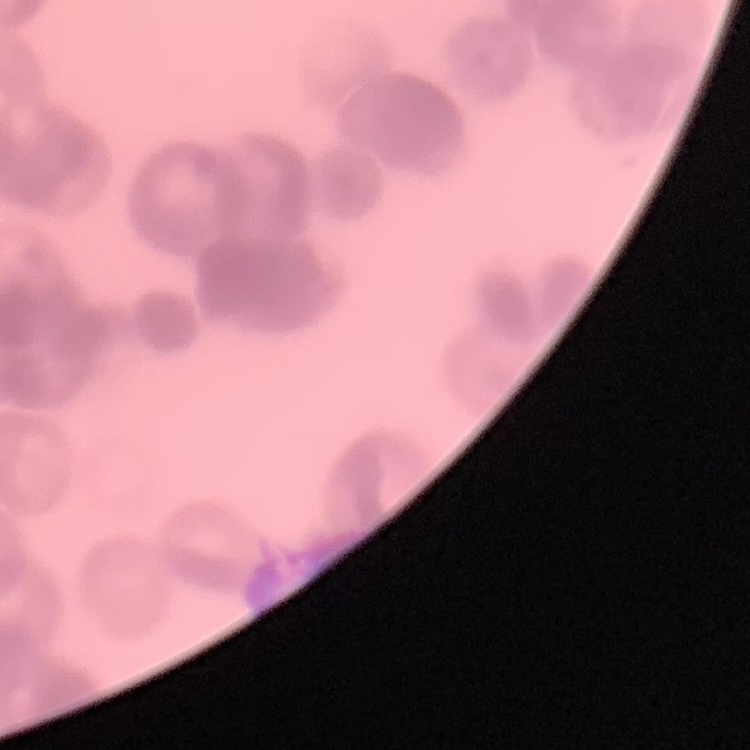

{
  "red_blood_cell_morphology": "rouleaux formation",
  "stain": "Field's or Giemsa",
  "image_type": "one tile cut from a larger photomicrograph",
  "preparation": "thin peripheral smear"
}